State which parasite is depicted.
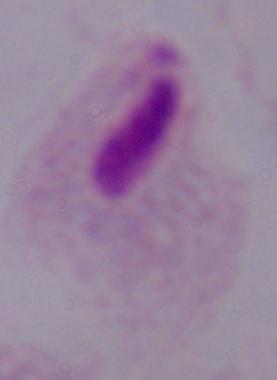
This is a trichomonad.

1000x magnification. Micrograph.